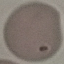

Malaria status: uninfected. Automatically extracted cell patch, resized to 64 × 64 pixels. Thin blood smear. Giemsa stain. Acquired by smartphone through the microscope eyepiece.